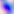

Summary:
  - Magnification: 400x
  - Modality: micrograph
  - Identification: Toxoplasma gondii